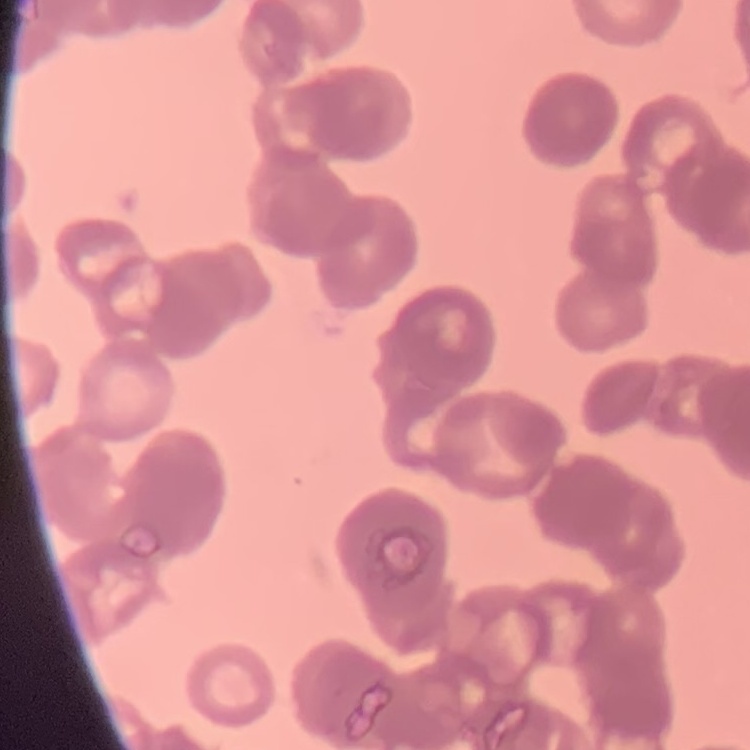
{
  "erythrocyte_morphology": "rouleaux formation",
  "stain": "Field's or Giemsa",
  "image_type": "one tile cut from a larger photomicrograph",
  "preparation": "thin blood film"
}